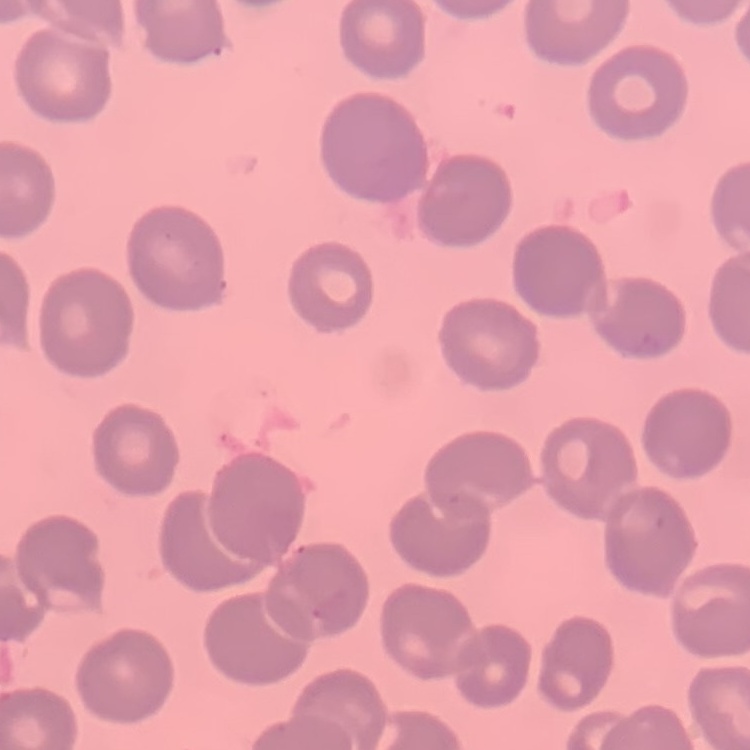

Summary:
  - Red blood cell morphology: no rouleaux formation
  - Stain: Field's or Giemsa
  - Preparation: thin blood film
  - Image type: one tile cut from a larger photomicrograph